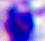

Summary:
  - Modality: micrograph
  - Identification: white blood cell
  - Magnification: 400x